Name the parasite shown.
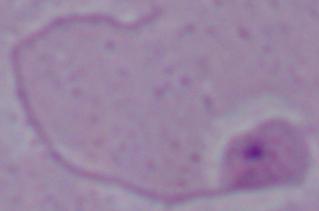

This is Leishmania.

Micrograph. 1000x magnification.